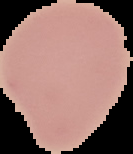

Malaria status: uninfected. Cell region segmented out of the field of view; the surrounding area is masked to black. Image is 133×154 pixels. From a thin blood smear.